Give the extent of all Plasmodium falciparum-infected red blood cells.
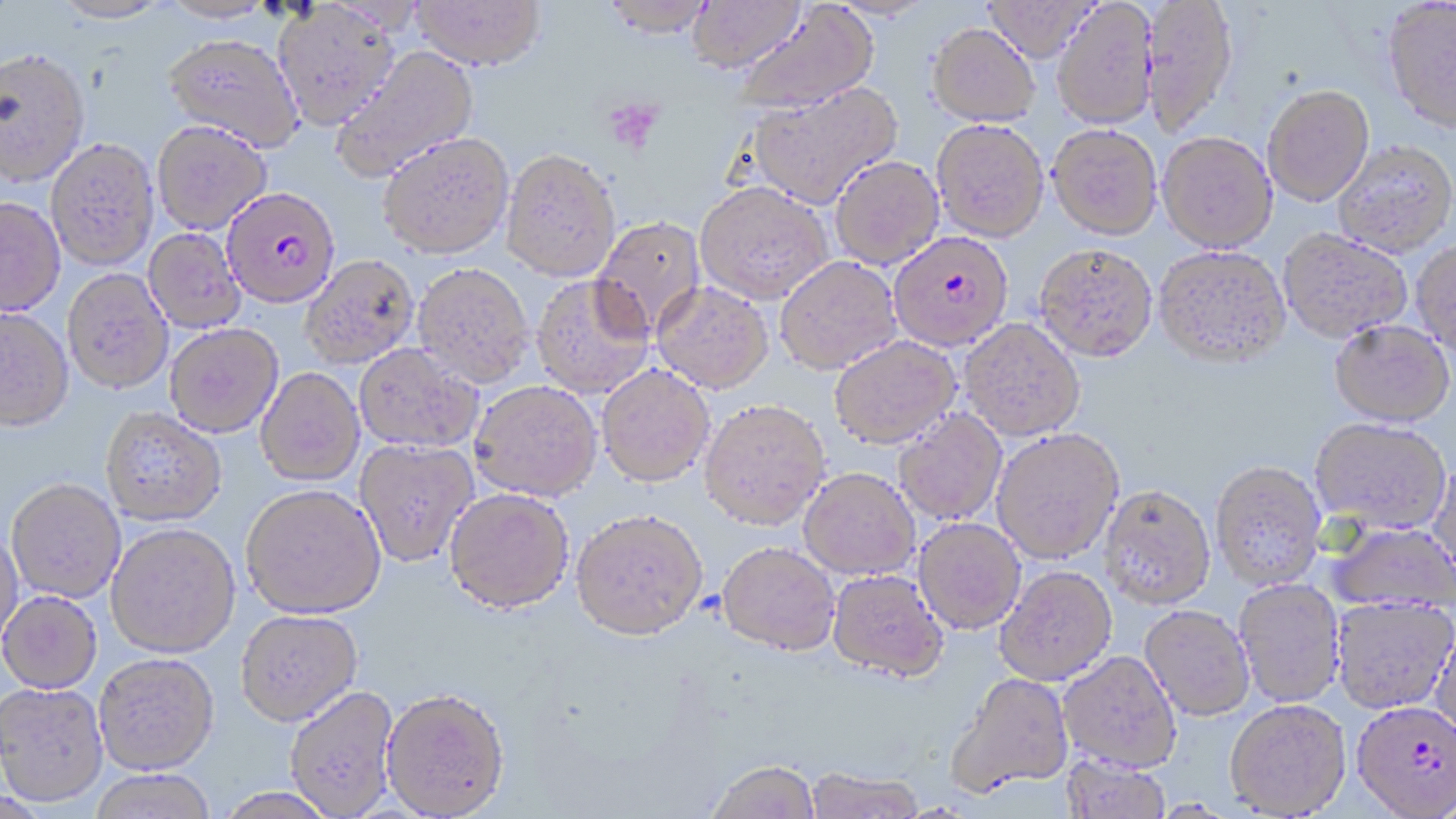
Approximate bounding boxes as named x1/y1/x2/y2 corners in pixels.
Plasmodium falciparum-infected red blood cells: (x1=222, y1=187, x2=341, y2=309), (x1=896, y1=233, x2=1016, y2=351), (x1=1351, y1=699, x2=1456, y2=817).

slide-level diagnosis = Plasmodium falciparum
preparation = thin blood film
image size = 1456×819 pixels
modality = light microscopy
platelet locations = approximate bounding boxes as named x1/y1/x2/y2 corners in pixels: (x1=603, y1=98, x2=664, y2=154)
stain = May-Grünwald-Giemsa
uninfected red blood cell locations = approximate bounding boxes as named x1/y1/x2/y2 corners in pixels: (x1=160, y1=0, x2=277, y2=25), (x1=412, y1=0, x2=545, y2=70), (x1=600, y1=0, x2=718, y2=37), (x1=982, y1=0, x2=1099, y2=62), (x1=1141, y1=0, x2=1240, y2=136), (x1=52, y1=1, x2=172, y2=25), (x1=684, y1=1, x2=806, y2=74), (x1=1052, y1=1, x2=1159, y2=129), (x1=1382, y1=1, x2=1456, y2=135), (x1=272, y1=2, x2=400, y2=130), (x1=732, y1=3, x2=879, y2=115), (x1=928, y1=22, x2=1040, y2=127), (x1=162, y1=34, x2=304, y2=152), (x1=329, y1=45, x2=479, y2=182), (x1=0, y1=51, x2=91, y2=190), (x1=746, y1=80, x2=902, y2=209), (x1=1263, y1=84, x2=1375, y2=206), (x1=931, y1=118, x2=1049, y2=242), (x1=152, y1=121, x2=272, y2=235), (x1=1048, y1=123, x2=1162, y2=239), (x1=1158, y1=131, x2=1277, y2=252), (x1=378, y1=132, x2=514, y2=259), (x1=46, y1=141, x2=159, y2=273), (x1=1333, y1=141, x2=1456, y2=258), (x1=500, y1=148, x2=621, y2=282), (x1=830, y1=155, x2=944, y2=269), (x1=695, y1=181, x2=833, y2=304), (x1=0, y1=200, x2=65, y2=319), (x1=591, y1=215, x2=707, y2=338), (x1=143, y1=228, x2=246, y2=334), (x1=1279, y1=230, x2=1412, y2=344), (x1=1411, y1=241, x2=1456, y2=356), (x1=1034, y1=243, x2=1158, y2=362), (x1=1153, y1=245, x2=1291, y2=369), (x1=301, y1=255, x2=419, y2=369), (x1=774, y1=255, x2=901, y2=374), (x1=413, y1=263, x2=534, y2=387), (x1=63, y1=271, x2=173, y2=396), (x1=531, y1=275, x2=654, y2=399), (x1=652, y1=281, x2=773, y2=393), (x1=0, y1=310, x2=74, y2=435), (x1=960, y1=318, x2=1085, y2=441), (x1=1329, y1=320, x2=1454, y2=428), (x1=164, y1=324, x2=283, y2=439), (x1=829, y1=336, x2=961, y2=449), (x1=354, y1=344, x2=483, y2=454), (x1=596, y1=364, x2=715, y2=487), (x1=256, y1=368, x2=364, y2=487), (x1=469, y1=380, x2=602, y2=501), (x1=699, y1=399, x2=830, y2=530), (x1=100, y1=409, x2=226, y2=528), (x1=894, y1=409, x2=1007, y2=526), (x1=1309, y1=418, x2=1450, y2=534), (x1=991, y1=428, x2=1124, y2=564), (x1=354, y1=439, x2=479, y2=568), (x1=1428, y1=457, x2=1456, y2=584), (x1=1210, y1=461, x2=1327, y2=590), (x1=799, y1=468, x2=920, y2=579), (x1=6, y1=481, x2=126, y2=605), (x1=1099, y1=485, x2=1216, y2=609), (x1=241, y1=486, x2=385, y2=621), (x1=444, y1=488, x2=574, y2=615), (x1=572, y1=508, x2=708, y2=640), (x1=914, y1=517, x2=1026, y2=634), (x1=1325, y1=522, x2=1455, y2=610), (x1=105, y1=525, x2=240, y2=660), (x1=0, y1=528, x2=24, y2=649), (x1=717, y1=541, x2=840, y2=655), (x1=995, y1=565, x2=1117, y2=684), (x1=827, y1=569, x2=949, y2=682), (x1=1234, y1=579, x2=1345, y2=707), (x1=0, y1=592, x2=102, y2=695), (x1=1330, y1=596, x2=1456, y2=714), (x1=1139, y1=605, x2=1255, y2=721), (x1=235, y1=610, x2=363, y2=727), (x1=1431, y1=621, x2=1456, y2=749), (x1=1058, y1=651, x2=1182, y2=772), (x1=94, y1=654, x2=219, y2=776), (x1=947, y1=672, x2=1075, y2=796), (x1=0, y1=683, x2=108, y2=809), (x1=285, y1=686, x2=400, y2=817), (x1=381, y1=688, x2=511, y2=818), (x1=1225, y1=699, x2=1351, y2=816), (x1=1060, y1=755, x2=1171, y2=819), (x1=707, y1=758, x2=821, y2=819), (x1=805, y1=767, x2=924, y2=818), (x1=87, y1=771, x2=217, y2=819), (x1=212, y1=788, x2=340, y2=819)
field of view = single
magnification = 1000x